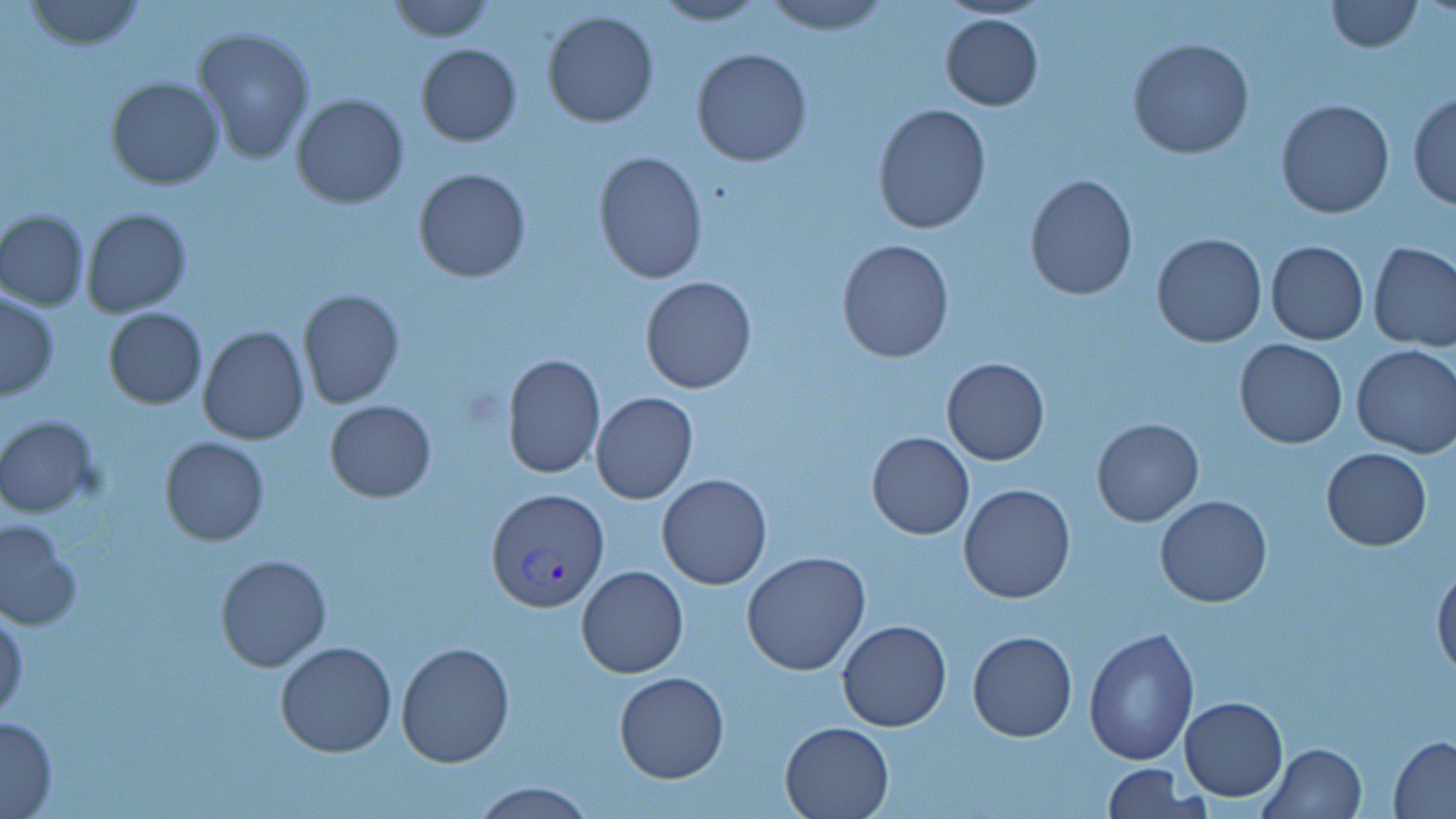

slide-level diagnosis = Plasmodium vivax
stain = May-Grünwald-Giemsa
image size = 1456×819 pixels
field of view = one of a larger specimen
uninfected red blood cell locations = approximate bounding boxes as [x1, y1, x2, y2] in pixels: [22, 0, 147, 51], [386, 0, 495, 41], [762, 0, 890, 34], [1324, 0, 1423, 53], [649, 1, 768, 26], [541, 9, 661, 128], [939, 12, 1043, 111], [192, 24, 316, 164], [1128, 38, 1254, 158], [416, 43, 522, 147], [691, 47, 812, 168], [106, 77, 226, 190], [1407, 91, 1456, 209], [291, 94, 410, 209], [1276, 99, 1395, 219], [872, 103, 993, 234], [593, 150, 708, 284], [413, 168, 532, 282], [1023, 174, 1138, 299], [81, 208, 192, 317], [0, 210, 89, 310], [1151, 232, 1267, 347], [836, 238, 954, 363], [1265, 240, 1369, 345], [1368, 242, 1456, 350], [640, 276, 756, 392], [297, 289, 405, 409], [1, 291, 59, 401], [102, 308, 207, 408], [197, 326, 308, 446], [1235, 338, 1348, 449], [1352, 345, 1456, 458], [502, 354, 604, 478], [942, 357, 1049, 465], [590, 392, 698, 506], [325, 399, 437, 502], [1, 415, 102, 518], [1091, 418, 1205, 527], [868, 431, 974, 539], [160, 437, 269, 546], [1321, 447, 1432, 551], [657, 474, 772, 589], [958, 483, 1076, 604], [1154, 495, 1272, 607], [0, 516, 82, 628], [741, 551, 871, 677], [215, 553, 332, 672], [1432, 559, 1456, 681], [577, 566, 688, 678], [0, 606, 26, 722], [836, 620, 953, 733], [1083, 625, 1199, 766], [967, 630, 1077, 742], [275, 640, 398, 757], [397, 641, 515, 766], [614, 672, 729, 783], [1179, 696, 1287, 802], [0, 713, 59, 817], [779, 721, 894, 818], [1389, 735, 1456, 817], [1260, 742, 1366, 819], [1102, 764, 1195, 818], [471, 781, 594, 818]
Plasmodium vivax-infected red blood cell locations = approximate bounding boxes as [x1, y1, x2, y2] in pixels: [486, 487, 609, 612]
magnification = 1000x
modality = optical microscopy
preparation = thin blood smear